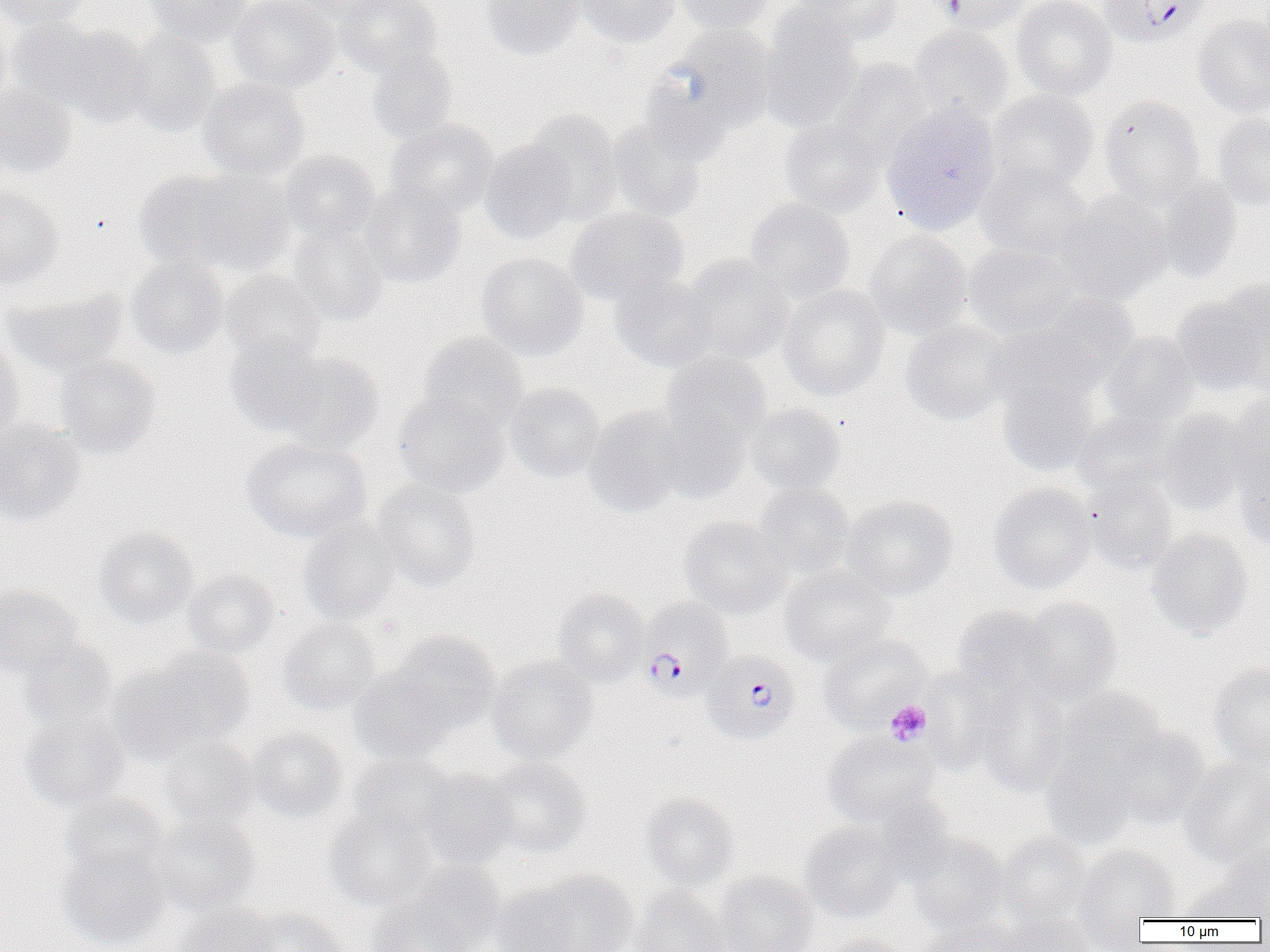
Approximate bounding boxes as named x1/y1/x2/y2 corners in pixels. Platelet locations: (x1=884, y1=699, x2=932, y2=746). Plasmodium falciparum-infected red blood cell locations: (x1=1100, y1=0, x2=1210, y2=47), (x1=639, y1=597, x2=735, y2=701), (x1=702, y1=651, x2=801, y2=746). Uninfected red blood cell locations: (x1=1, y1=0, x2=90, y2=30), (x1=144, y1=0, x2=251, y2=48), (x1=227, y1=0, x2=340, y2=92), (x1=291, y1=0, x2=399, y2=25), (x1=337, y1=0, x2=440, y2=78), (x1=479, y1=0, x2=586, y2=60), (x1=575, y1=0, x2=680, y2=47), (x1=673, y1=0, x2=776, y2=34), (x1=794, y1=0, x2=903, y2=47), (x1=930, y1=0, x2=1032, y2=35), (x1=1012, y1=0, x2=1117, y2=100), (x1=0, y1=10, x2=13, y2=108), (x1=759, y1=10, x2=862, y2=132), (x1=1193, y1=15, x2=1270, y2=118), (x1=38, y1=23, x2=155, y2=126), (x1=908, y1=25, x2=1015, y2=121), (x1=664, y1=26, x2=779, y2=136), (x1=122, y1=30, x2=221, y2=137), (x1=366, y1=49, x2=459, y2=144), (x1=826, y1=58, x2=930, y2=156), (x1=199, y1=77, x2=309, y2=181), (x1=638, y1=78, x2=731, y2=167), (x1=0, y1=82, x2=78, y2=177), (x1=987, y1=90, x2=1098, y2=193), (x1=1098, y1=95, x2=1206, y2=205), (x1=882, y1=104, x2=1001, y2=235), (x1=522, y1=110, x2=623, y2=225), (x1=781, y1=113, x2=890, y2=217), (x1=1212, y1=114, x2=1270, y2=210), (x1=385, y1=118, x2=498, y2=218), (x1=606, y1=118, x2=709, y2=221), (x1=479, y1=138, x2=578, y2=244), (x1=279, y1=150, x2=380, y2=244), (x1=976, y1=162, x2=1093, y2=260), (x1=133, y1=168, x2=266, y2=274), (x1=1151, y1=176, x2=1242, y2=282), (x1=359, y1=181, x2=466, y2=288), (x1=0, y1=185, x2=63, y2=288), (x1=1056, y1=193, x2=1173, y2=303), (x1=745, y1=198, x2=855, y2=303), (x1=567, y1=206, x2=689, y2=304), (x1=287, y1=223, x2=389, y2=325), (x1=865, y1=230, x2=972, y2=339), (x1=963, y1=242, x2=1080, y2=338), (x1=476, y1=252, x2=588, y2=360), (x1=681, y1=255, x2=794, y2=363), (x1=126, y1=257, x2=230, y2=359), (x1=220, y1=270, x2=325, y2=369), (x1=611, y1=276, x2=720, y2=372), (x1=779, y1=285, x2=889, y2=400), (x1=1172, y1=286, x2=1269, y2=396), (x1=3, y1=287, x2=129, y2=377), (x1=1009, y1=293, x2=1141, y2=394), (x1=900, y1=319, x2=1015, y2=425), (x1=1100, y1=331, x2=1199, y2=428), (x1=417, y1=332, x2=529, y2=432), (x1=224, y1=334, x2=327, y2=437), (x1=0, y1=337, x2=25, y2=443), (x1=273, y1=352, x2=385, y2=454), (x1=661, y1=352, x2=772, y2=449), (x1=55, y1=355, x2=161, y2=458), (x1=997, y1=374, x2=1102, y2=476), (x1=505, y1=383, x2=604, y2=482), (x1=393, y1=391, x2=510, y2=497), (x1=1222, y1=395, x2=1270, y2=500), (x1=746, y1=403, x2=846, y2=496), (x1=584, y1=404, x2=691, y2=517), (x1=1072, y1=409, x2=1180, y2=499), (x1=1156, y1=409, x2=1252, y2=514), (x1=650, y1=413, x2=749, y2=503), (x1=0, y1=420, x2=86, y2=526), (x1=242, y1=437, x2=372, y2=543), (x1=1235, y1=450, x2=1270, y2=552), (x1=1082, y1=477, x2=1179, y2=575), (x1=371, y1=479, x2=482, y2=591), (x1=988, y1=481, x2=1097, y2=594), (x1=754, y1=482, x2=854, y2=578), (x1=841, y1=494, x2=959, y2=601), (x1=679, y1=516, x2=792, y2=619), (x1=298, y1=518, x2=400, y2=627), (x1=94, y1=526, x2=199, y2=627), (x1=1146, y1=527, x2=1252, y2=640), (x1=779, y1=565, x2=896, y2=665), (x1=182, y1=569, x2=280, y2=659), (x1=0, y1=585, x2=82, y2=675), (x1=552, y1=587, x2=649, y2=686), (x1=1018, y1=597, x2=1123, y2=704), (x1=952, y1=605, x2=1058, y2=699), (x1=276, y1=617, x2=381, y2=715), (x1=385, y1=630, x2=500, y2=731), (x1=817, y1=634, x2=931, y2=732), (x1=18, y1=638, x2=118, y2=733), (x1=109, y1=651, x2=250, y2=764), (x1=487, y1=655, x2=599, y2=765), (x1=1208, y1=663, x2=1270, y2=769), (x1=918, y1=670, x2=1001, y2=775), (x1=349, y1=671, x2=455, y2=765), (x1=973, y1=680, x2=1073, y2=795), (x1=1053, y1=686, x2=1168, y2=779), (x1=20, y1=710, x2=130, y2=814), (x1=1099, y1=724, x2=1210, y2=830), (x1=248, y1=726, x2=348, y2=824), (x1=821, y1=731, x2=939, y2=828), (x1=158, y1=736, x2=260, y2=833), (x1=1039, y1=741, x2=1145, y2=849), (x1=346, y1=753, x2=458, y2=841), (x1=1179, y1=755, x2=1270, y2=868), (x1=483, y1=757, x2=591, y2=859), (x1=418, y1=769, x2=518, y2=869), (x1=640, y1=792, x2=740, y2=891), (x1=61, y1=793, x2=172, y2=887), (x1=323, y1=805, x2=437, y2=910), (x1=146, y1=812, x2=260, y2=917), (x1=800, y1=820, x2=905, y2=923), (x1=995, y1=831, x2=1095, y2=928), (x1=908, y1=833, x2=1010, y2=938), (x1=55, y1=843, x2=171, y2=950), (x1=1073, y1=845, x2=1182, y2=927), (x1=386, y1=860, x2=508, y2=952), (x1=505, y1=869, x2=640, y2=952), (x1=711, y1=871, x2=818, y2=952), (x1=1179, y1=872, x2=1270, y2=922), (x1=631, y1=885, x2=730, y2=952), (x1=172, y1=903, x2=282, y2=952), (x1=244, y1=906, x2=348, y2=952), (x1=997, y1=911, x2=1097, y2=952), (x1=919, y1=920, x2=1025, y2=952), (x1=818, y1=933, x2=910, y2=952). Slide-level diagnosis: Plasmodium falciparum. Thin blood smear. Light microscopy. One field of a larger specimen. 1000x magnification. Image is 1270×952 pixels.